Assess this cell for malaria.
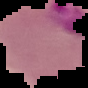

Parasitized.

The area outside the segmented cell region is set to black. From a thin blood smear. Image is 88×88 pixels.